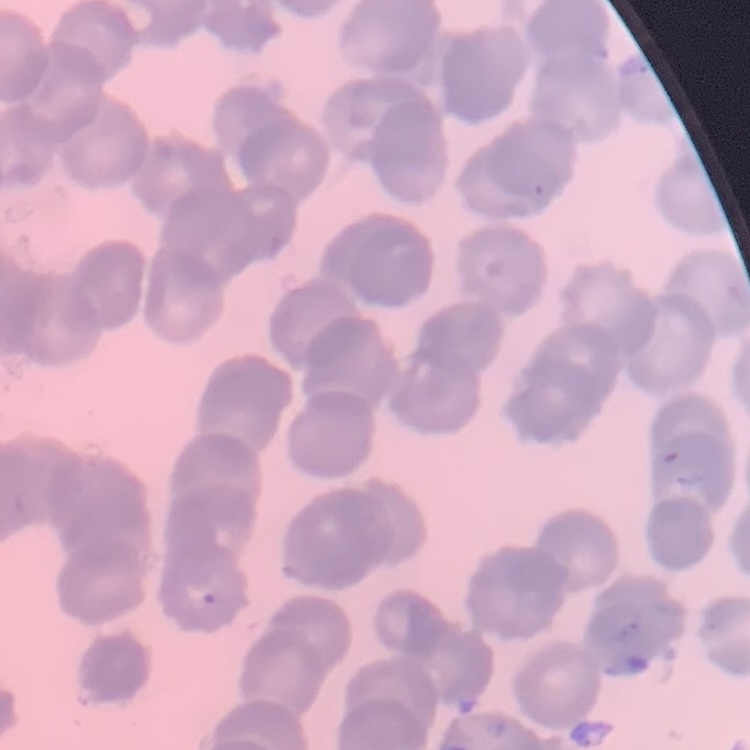 The erythrocytes show rouleaux formation. Stained with either Field's or Giemsa. Thin blood film. One tile cut from a larger photomicrograph.